Locate and identify every blood parasite.
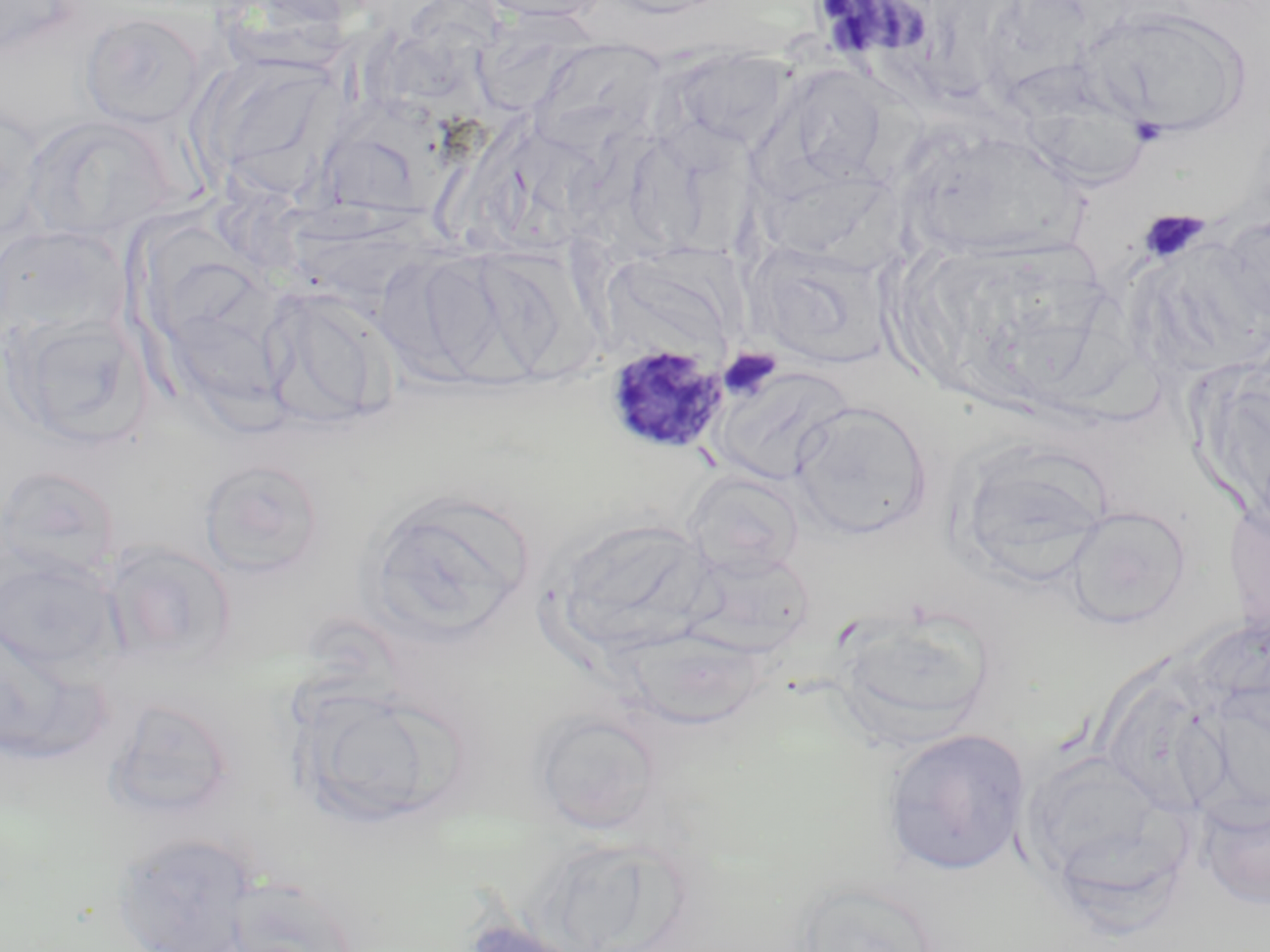

Approximate bounding boxes as [x1, y1, x2, y2] in pixels.
Plasmodium malariae-infected red blood cells: [603, 342, 730, 457].
No Plasmodium falciparum, Plasmodium ovale, Plasmodium vivax, Babesia divergens, or Trypanosoma brucei observed.

{
  "slide_level_diagnosis": "Plasmodium malariae",
  "platelet_locations": "approximate bounding boxes as [x1, y1, x2, y2] in pixels: [1129, 117, 1168, 147], [1139, 210, 1209, 266], [718, 347, 782, 402]",
  "magnification": "1000x",
  "modality": "light microscopy",
  "field_of_view": "one of a larger specimen",
  "image_size": "1270×952 pixels",
  "uninfected_red_blood_cell_locations": "approximate bounding boxes as [x1, y1, x2, y2] in pixels: [470, 0, 613, 24], [593, 0, 735, 18], [0, 1, 78, 58], [1083, 7, 1252, 138], [80, 10, 208, 129], [529, 39, 668, 149], [672, 47, 794, 152], [195, 57, 335, 197], [780, 64, 892, 187], [1, 101, 45, 248], [25, 115, 177, 244], [624, 119, 756, 256], [922, 147, 1093, 267], [1217, 212, 1270, 332], [0, 224, 130, 338], [752, 241, 894, 370], [465, 246, 583, 378], [168, 266, 306, 402], [260, 285, 397, 429], [6, 312, 153, 448], [713, 365, 852, 486], [790, 400, 932, 540], [949, 440, 1115, 588], [199, 458, 327, 579], [0, 464, 122, 582], [683, 470, 804, 580], [364, 490, 536, 642], [1226, 500, 1270, 651], [1063, 505, 1192, 630], [550, 516, 717, 661], [101, 539, 238, 666], [682, 547, 815, 658], [0, 553, 121, 674], [832, 610, 1000, 746], [0, 622, 114, 766], [619, 627, 770, 729], [293, 683, 451, 827], [103, 695, 240, 821], [533, 708, 665, 833], [883, 727, 1031, 876], [1019, 750, 1192, 908], [1197, 790, 1270, 911], [111, 831, 259, 952], [220, 876, 363, 952], [789, 879, 945, 952], [457, 918, 591, 952]",
  "stain": "May-Grünwald-Giemsa",
  "preparation": "thin blood film"
}